Report the malaria status of this cell.
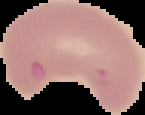
It is parasitized.

Summary:
  - Preparation: thin blood smear
  - Image type: segmented cell region with the area outside set to black
  - Image size: 145×115 pixels